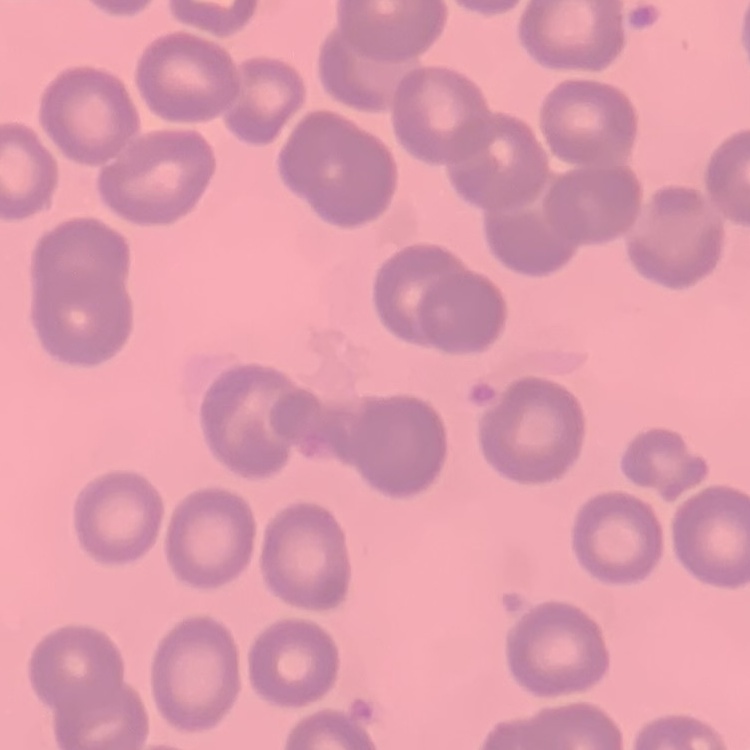
erythrocyte morphology = no rouleaux formation
stain = Field's or Giemsa
image type = square crop of a larger photomicrograph
preparation = thin peripheral smear